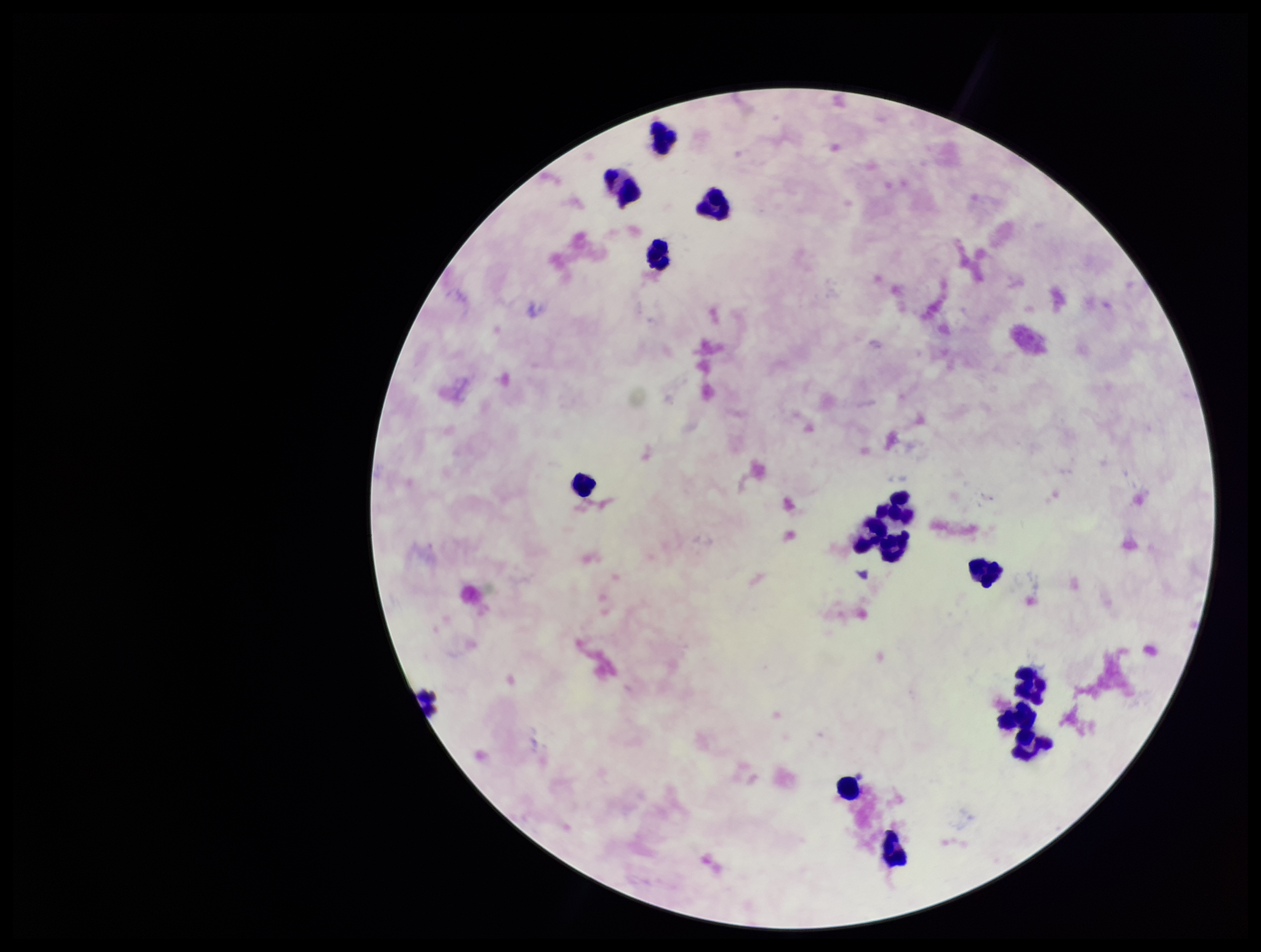
Summary:
  - Parasite count: 0
  - Leukocyte count: 15
  - Preparation: thick blood smear
  - Stain: Giemsa
  - Field of view: one from this slide
  - Capture: smartphone photograph through the microscope eyepiece
  - Image size: 1261×952 pixels
  - Patient malaria status: negative
  - Plasmodium parasites: none identified